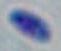 Micrograph. Toxoplasma gondii is shown. 1000x magnification.